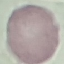
{
  "result": "negative for malaria parasites",
  "image_type": "automatically extracted cell patch, resized to 64 × 64 pixels",
  "preparation": "thin blood film",
  "stain": "Giemsa",
  "capture": "smartphone camera at the microscope eyepiece"
}